Outline each Plasmodium falciparum-infected red blood cell.
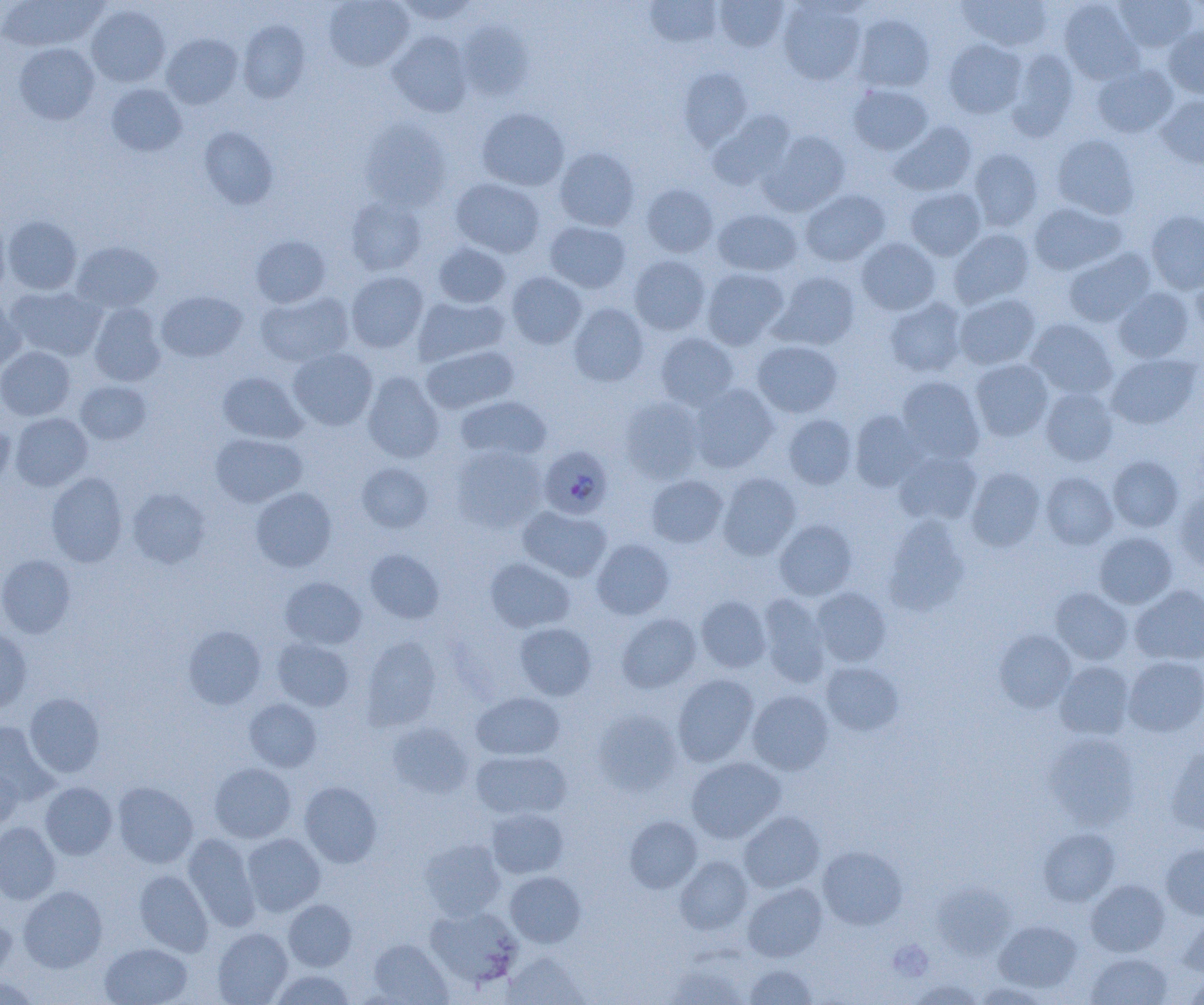
Approximate bounding boxes as named x1/y1/x2/y2 corners in pixels.
Plasmodium falciparum-infected red blood cells: (x1=539, y1=446, x2=613, y2=519).

Summary:
  - Platelet locations: (x1=890, y1=938, x2=937, y2=981)
  - Uninfected red blood cell locations: (x1=324, y1=0, x2=414, y2=71), (x1=395, y1=0, x2=479, y2=24), (x1=643, y1=0, x2=722, y2=48), (x1=959, y1=0, x2=1053, y2=51), (x1=1114, y1=0, x2=1197, y2=52), (x1=0, y1=1, x2=107, y2=52), (x1=715, y1=1, x2=788, y2=52), (x1=1059, y1=1, x2=1143, y2=84), (x1=778, y1=2, x2=866, y2=85), (x1=86, y1=5, x2=170, y2=87), (x1=853, y1=14, x2=935, y2=93), (x1=238, y1=20, x2=309, y2=102), (x1=458, y1=20, x2=532, y2=102), (x1=1164, y1=26, x2=1204, y2=99), (x1=387, y1=31, x2=472, y2=117), (x1=162, y1=34, x2=243, y2=109), (x1=943, y1=39, x2=1026, y2=118), (x1=14, y1=43, x2=99, y2=124), (x1=1006, y1=48, x2=1079, y2=140), (x1=1092, y1=63, x2=1178, y2=137), (x1=678, y1=67, x2=753, y2=149), (x1=107, y1=84, x2=186, y2=156), (x1=848, y1=84, x2=933, y2=155), (x1=1156, y1=95, x2=1204, y2=168), (x1=476, y1=108, x2=569, y2=191), (x1=709, y1=111, x2=795, y2=191), (x1=360, y1=118, x2=452, y2=210), (x1=890, y1=121, x2=977, y2=196), (x1=199, y1=126, x2=278, y2=209), (x1=763, y1=130, x2=850, y2=215), (x1=1051, y1=134, x2=1140, y2=219), (x1=554, y1=147, x2=639, y2=231), (x1=968, y1=148, x2=1043, y2=231), (x1=450, y1=178, x2=544, y2=258), (x1=641, y1=184, x2=718, y2=257), (x1=905, y1=187, x2=985, y2=261), (x1=800, y1=189, x2=890, y2=266), (x1=346, y1=197, x2=427, y2=275), (x1=1029, y1=202, x2=1126, y2=275), (x1=712, y1=208, x2=802, y2=276), (x1=1146, y1=210, x2=1204, y2=294), (x1=0, y1=213, x2=11, y2=297), (x1=3, y1=215, x2=82, y2=295), (x1=544, y1=221, x2=631, y2=293), (x1=949, y1=229, x2=1034, y2=308), (x1=251, y1=235, x2=331, y2=307), (x1=857, y1=238, x2=941, y2=315), (x1=71, y1=241, x2=163, y2=313), (x1=432, y1=242, x2=510, y2=308), (x1=1062, y1=247, x2=1156, y2=327), (x1=628, y1=255, x2=711, y2=335), (x1=1190, y1=266, x2=1204, y2=342), (x1=701, y1=268, x2=789, y2=350), (x1=346, y1=271, x2=428, y2=353), (x1=772, y1=271, x2=860, y2=350), (x1=506, y1=272, x2=587, y2=349), (x1=6, y1=285, x2=106, y2=361), (x1=1113, y1=287, x2=1194, y2=363), (x1=156, y1=291, x2=247, y2=362), (x1=256, y1=292, x2=354, y2=367), (x1=954, y1=293, x2=1040, y2=370), (x1=0, y1=295, x2=25, y2=372), (x1=413, y1=296, x2=508, y2=366), (x1=885, y1=297, x2=967, y2=377), (x1=88, y1=303, x2=166, y2=387), (x1=568, y1=303, x2=649, y2=386), (x1=1026, y1=319, x2=1117, y2=400), (x1=655, y1=332, x2=739, y2=410), (x1=752, y1=340, x2=843, y2=417), (x1=421, y1=345, x2=519, y2=414), (x1=0, y1=347, x2=76, y2=420), (x1=288, y1=347, x2=378, y2=430), (x1=1107, y1=353, x2=1200, y2=429), (x1=970, y1=359, x2=1053, y2=441), (x1=218, y1=371, x2=306, y2=444), (x1=363, y1=372, x2=445, y2=463), (x1=897, y1=376, x2=985, y2=464), (x1=75, y1=381, x2=151, y2=445), (x1=688, y1=383, x2=779, y2=473), (x1=1040, y1=388, x2=1118, y2=465), (x1=455, y1=395, x2=552, y2=462), (x1=620, y1=397, x2=704, y2=482), (x1=850, y1=411, x2=925, y2=492), (x1=10, y1=413, x2=93, y2=491), (x1=784, y1=414, x2=857, y2=489), (x1=0, y1=419, x2=15, y2=491), (x1=210, y1=433, x2=307, y2=507), (x1=451, y1=445, x2=547, y2=532), (x1=894, y1=450, x2=982, y2=526), (x1=1108, y1=456, x2=1183, y2=532), (x1=356, y1=462, x2=433, y2=533), (x1=966, y1=467, x2=1045, y2=552), (x1=1041, y1=471, x2=1118, y2=550), (x1=47, y1=472, x2=127, y2=567), (x1=718, y1=473, x2=801, y2=559), (x1=647, y1=474, x2=728, y2=548), (x1=251, y1=486, x2=336, y2=571), (x1=127, y1=488, x2=211, y2=568), (x1=1174, y1=489, x2=1204, y2=571), (x1=518, y1=505, x2=611, y2=581), (x1=884, y1=515, x2=970, y2=614), (x1=774, y1=520, x2=857, y2=601), (x1=1094, y1=532, x2=1177, y2=609), (x1=592, y1=539, x2=674, y2=619), (x1=364, y1=548, x2=444, y2=624), (x1=0, y1=554, x2=77, y2=638), (x1=485, y1=557, x2=575, y2=633), (x1=279, y1=576, x2=366, y2=649), (x1=1131, y1=585, x2=1204, y2=665), (x1=812, y1=587, x2=892, y2=666), (x1=1050, y1=588, x2=1132, y2=665), (x1=695, y1=594, x2=772, y2=673), (x1=758, y1=594, x2=831, y2=686), (x1=617, y1=613, x2=702, y2=693), (x1=514, y1=622, x2=596, y2=700), (x1=183, y1=625, x2=266, y2=710), (x1=0, y1=626, x2=32, y2=712), (x1=994, y1=630, x2=1075, y2=713), (x1=360, y1=636, x2=442, y2=730), (x1=272, y1=637, x2=355, y2=712), (x1=1123, y1=656, x2=1204, y2=736), (x1=821, y1=661, x2=904, y2=736), (x1=1055, y1=661, x2=1135, y2=740), (x1=672, y1=674, x2=759, y2=766), (x1=747, y1=690, x2=833, y2=774), (x1=471, y1=692, x2=564, y2=760), (x1=24, y1=693, x2=105, y2=777), (x1=244, y1=698, x2=322, y2=772), (x1=592, y1=709, x2=683, y2=796), (x1=0, y1=721, x2=57, y2=805), (x1=387, y1=721, x2=473, y2=798), (x1=1045, y1=734, x2=1140, y2=830), (x1=1167, y1=746, x2=1204, y2=836), (x1=471, y1=750, x2=571, y2=820), (x1=686, y1=757, x2=785, y2=843), (x1=209, y1=762, x2=296, y2=843), (x1=0, y1=764, x2=22, y2=829), (x1=299, y1=781, x2=382, y2=867), (x1=40, y1=782, x2=117, y2=859), (x1=112, y1=782, x2=198, y2=868), (x1=486, y1=808, x2=568, y2=878), (x1=738, y1=811, x2=825, y2=893), (x1=624, y1=815, x2=702, y2=893), (x1=0, y1=821, x2=61, y2=903), (x1=1038, y1=828, x2=1120, y2=905), (x1=183, y1=833, x2=261, y2=931), (x1=241, y1=833, x2=326, y2=916), (x1=420, y1=838, x2=506, y2=920), (x1=1160, y1=844, x2=1204, y2=919), (x1=817, y1=845, x2=907, y2=929), (x1=675, y1=856, x2=753, y2=935), (x1=135, y1=869, x2=213, y2=956), (x1=505, y1=871, x2=585, y2=947), (x1=1086, y1=879, x2=1170, y2=956), (x1=742, y1=883, x2=827, y2=961), (x1=933, y1=883, x2=1015, y2=959), (x1=18, y1=886, x2=107, y2=972), (x1=284, y1=899, x2=356, y2=971), (x1=425, y1=906, x2=523, y2=989), (x1=0, y1=915, x2=16, y2=983), (x1=1178, y1=915, x2=1204, y2=976), (x1=994, y1=919, x2=1082, y2=992), (x1=213, y1=927, x2=293, y2=1005), (x1=368, y1=939, x2=453, y2=1004), (x1=100, y1=942, x2=192, y2=1005), (x1=503, y1=952, x2=591, y2=1004), (x1=1086, y1=952, x2=1173, y2=1005), (x1=665, y1=959, x2=748, y2=1005), (x1=744, y1=963, x2=818, y2=1005), (x1=271, y1=969, x2=355, y2=1005), (x1=1182, y1=972, x2=1204, y2=1004), (x1=0, y1=975, x2=43, y2=1005), (x1=907, y1=978, x2=985, y2=1005), (x1=974, y1=981, x2=1052, y2=1004)
  - Slide-level diagnosis: Plasmodium falciparum
  - Magnification: 1000x
  - Modality: optical microscopy
  - Image size: 1204×1005 pixels
  - Preparation: thin blood film
  - Field of view: single